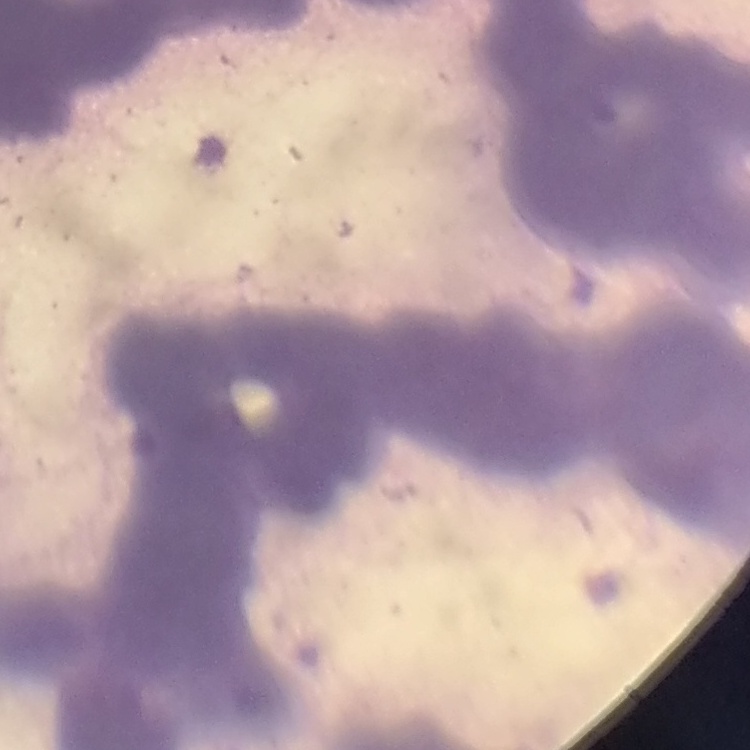

Summary:
  - Red blood cell morphology: rouleaux formation
  - Stain: Field's or Giemsa
  - Image type: square crop of a larger photomicrograph
  - Preparation: thin blood smear